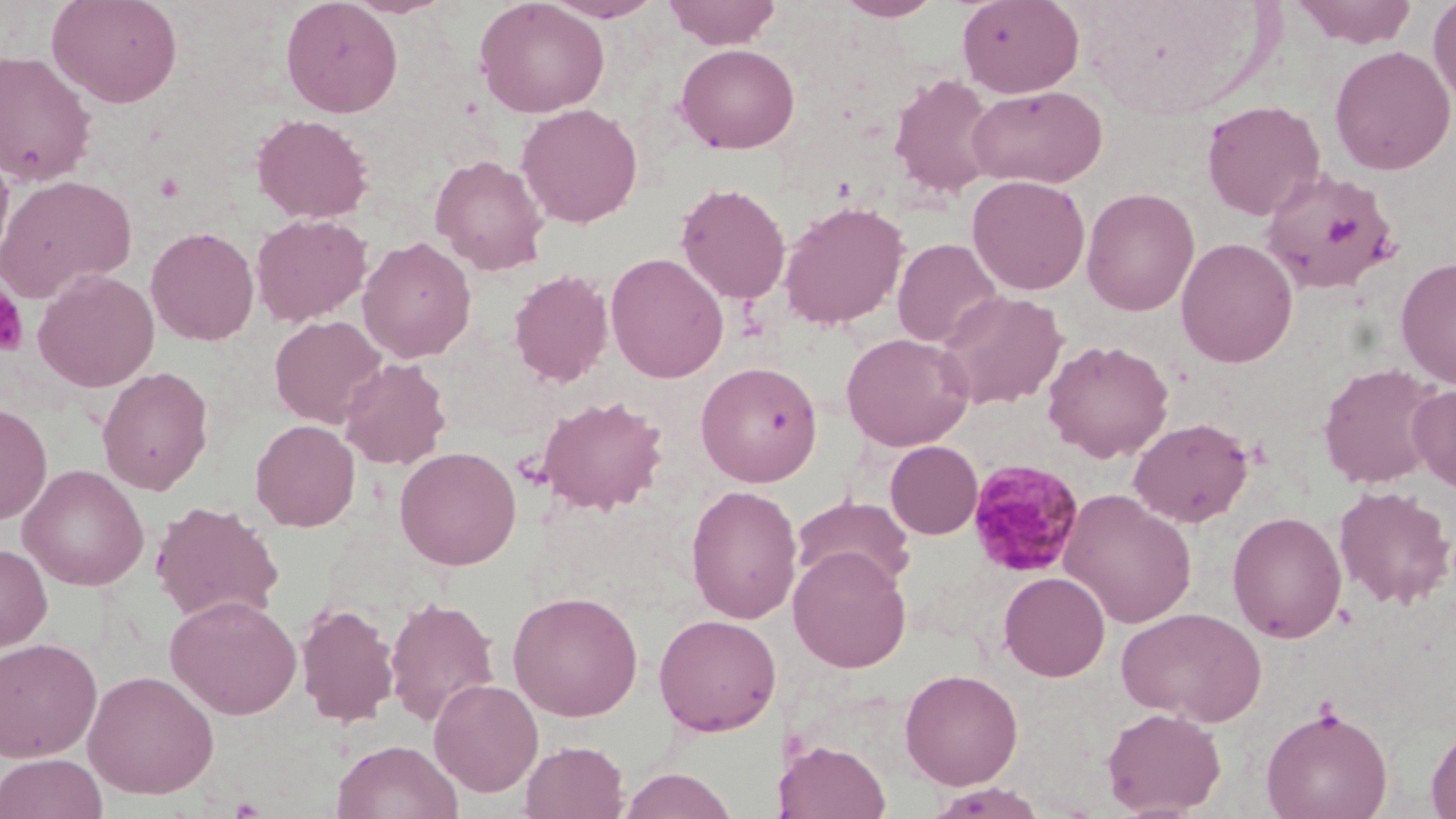

Summary:
  - Coordinate format: approximate bounding boxes as (x1, y1, x2, y2) in pixels
  - Plasmodium malariae-infected red blood cell locations: (968, 458, 1086, 579)
  - Platelet locations: (154, 172, 186, 202), (0, 282, 29, 358)
  - Uninfected red blood cell locations: (47, 0, 184, 108), (280, 0, 403, 117), (475, 0, 610, 118), (542, 0, 665, 22), (663, 0, 782, 49), (834, 0, 946, 21), (957, 0, 1084, 98), (1293, 0, 1417, 49), (1428, 0, 1456, 107), (675, 43, 800, 154), (1329, 45, 1455, 175), (0, 50, 97, 188), (888, 73, 999, 199), (967, 85, 1107, 188), (1200, 100, 1325, 221), (516, 103, 643, 228), (251, 113, 374, 223), (0, 144, 15, 271), (429, 154, 549, 275), (1260, 167, 1399, 295), (967, 174, 1091, 294), (0, 175, 137, 304), (675, 182, 791, 305), (1082, 187, 1200, 316), (778, 200, 909, 330), (251, 213, 372, 327), (145, 226, 260, 346), (357, 236, 476, 363), (1175, 237, 1299, 367), (892, 238, 1002, 349), (606, 252, 729, 384), (1395, 256, 1456, 389), (32, 268, 160, 392), (508, 269, 613, 387), (935, 290, 1068, 410), (269, 316, 387, 428), (841, 332, 973, 451), (1042, 339, 1175, 462), (339, 358, 451, 470), (696, 361, 823, 487), (1317, 362, 1445, 489), (97, 366, 214, 495), (1407, 383, 1456, 494), (535, 394, 669, 515), (0, 403, 53, 525), (1128, 417, 1254, 528), (250, 419, 361, 531), (885, 441, 983, 539), (394, 445, 522, 570), (18, 464, 149, 591), (685, 484, 802, 624), (1333, 485, 1455, 609), (1059, 489, 1197, 629), (791, 495, 915, 593), (150, 500, 285, 624), (1227, 511, 1347, 643), (0, 542, 53, 653), (788, 547, 912, 672), (998, 571, 1110, 681), (507, 590, 643, 722), (165, 593, 302, 720), (384, 596, 501, 728), (295, 603, 400, 727), (1117, 606, 1267, 726), (653, 613, 782, 736), (0, 637, 103, 763), (899, 668, 1023, 789), (83, 669, 219, 799), (428, 678, 544, 796), (1261, 704, 1394, 819), (1102, 706, 1226, 817), (1425, 719, 1456, 819), (331, 738, 464, 819), (776, 739, 891, 819), (520, 740, 628, 818), (0, 753, 107, 819), (619, 768, 738, 819), (926, 783, 1048, 819)
  - Slide-level diagnosis: Plasmodium malariae
  - Preparation: thin blood smear
  - Magnification: 1000x
  - Modality: optical microscopy
  - Image size: 1456×819 pixels
  - Field of view: single
  - Stain: May-Grünwald-Giemsa